Locate every parasitized RBC.
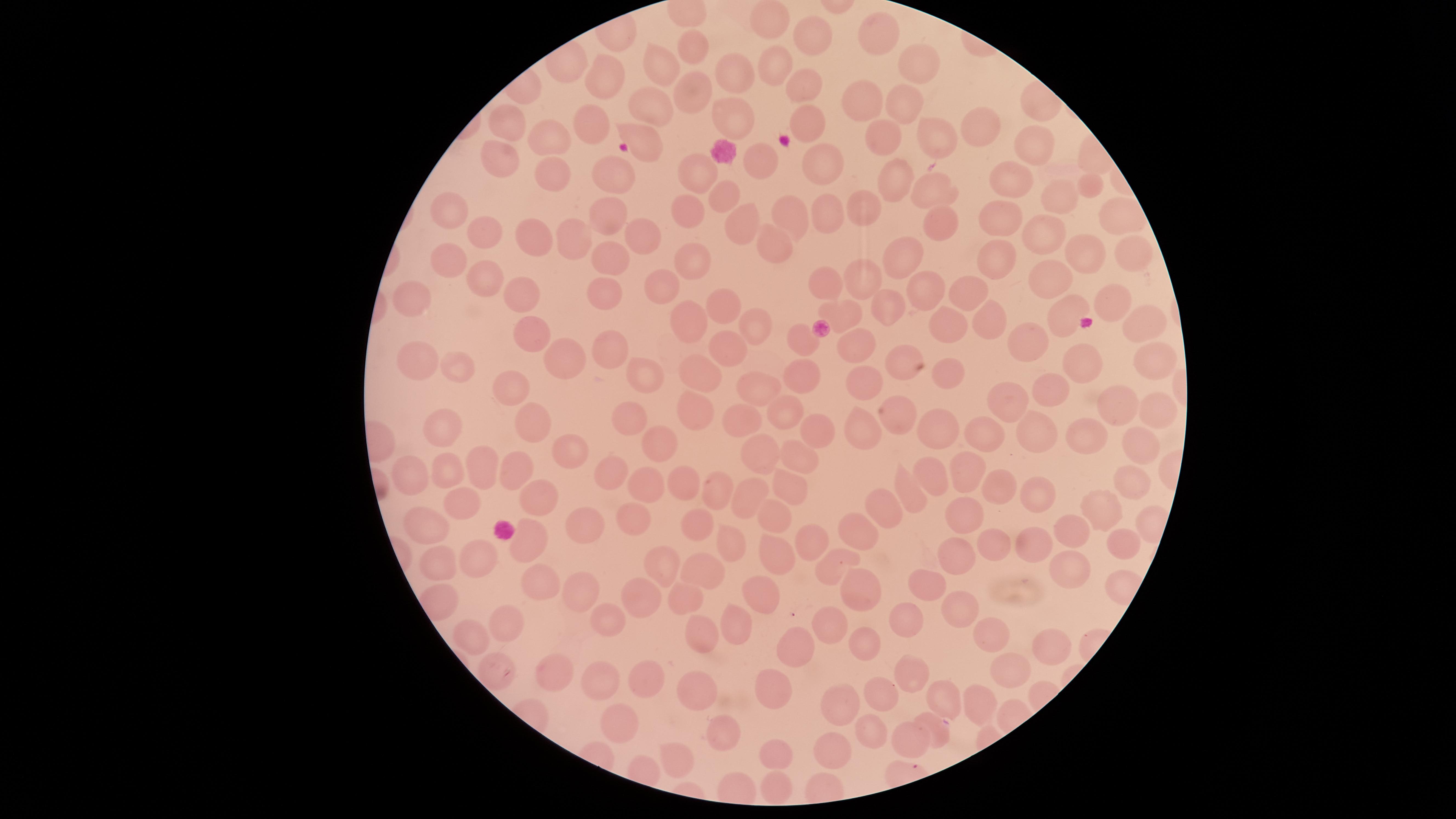

Approximate marker points as {x, y} in pixels.
Parasitized RBCs: {936, 729}.

Approximate marker points as {x, y} in pixels. Uninfected RBCs: {768, 20}, {882, 32}, {815, 36}, {690, 44}, {914, 61}, {657, 64}, {774, 67}, {724, 75}, {598, 79}, {804, 82}, {691, 91}, {865, 95}, {902, 99}, {646, 105}, {727, 119}, {513, 121}, {810, 122}, {592, 126}, {976, 126}, {885, 137}, {548, 139}, {1033, 139}, {940, 140}, {650, 141}, {499, 151}, {760, 158}, {823, 161}, {553, 171}, {700, 176}, {895, 176}, {619, 180}, {1016, 184}, {1087, 184}, {944, 188}, {726, 198}, {1062, 199}, {452, 205}, {868, 205}, {798, 207}, {690, 208}, {827, 208}, {1003, 211}, {599, 213}, {1120, 215}, {945, 219}, {745, 220}, {491, 230}, {1042, 233}, {640, 234}, {530, 235}, {780, 239}, {577, 242}, {1131, 242}, {452, 252}, {1079, 252}, {902, 253}, {613, 258}, {696, 263}, {1003, 264}, {481, 273}, {866, 273}, {1055, 278}, {828, 284}, {660, 286}, {924, 286}, {512, 290}, {975, 292}, {409, 295}, {601, 296}, {1116, 302}, {715, 306}, {885, 307}, {850, 308}, {1063, 309}, {992, 315}, {756, 318}, {1139, 319}, {691, 321}, {952, 321}, {531, 336}, {1037, 340}, {803, 341}, {729, 343}, {864, 344}, {614, 348}, {902, 358}, {1157, 358}, {568, 359}, {418, 362}, {459, 363}, {1090, 363}, {703, 369}, {952, 370}, {648, 372}, {807, 373}, {864, 380}, {511, 385}, {757, 385}, {1050, 388}, {1114, 404}, {1010, 407}, {697, 410}, {1157, 410}, {788, 413}, {900, 416}, {622, 419}, {439, 421}, {539, 421}, {742, 421}, {935, 428}, {860, 429}, {1088, 429}, {816, 434}, {1032, 434}, {986, 437}, {1132, 440}, {658, 442}, {566, 451}, {762, 453}, {799, 453}, {478, 463}, {964, 469}, {932, 470}, {614, 471}, {509, 473}, {1129, 473}, {443, 474}, {415, 475}, {679, 475}, {645, 481}, {996, 481}, {786, 484}, {712, 489}, {1038, 492}, {906, 493}, {746, 498}, {466, 505}, {538, 505}, {882, 507}, {1103, 508}, {966, 514}, {635, 517}, {780, 517}, {701, 525}, {428, 526}, {1081, 526}, {579, 527}, {858, 532}, {729, 537}, {812, 538}, {1120, 541}, {520, 542}, {994, 543}, {1038, 548}, {772, 557}, {475, 559}, {955, 559}, {664, 562}, {439, 565}, {826, 565}, {701, 569}, {1068, 569}, {536, 581}, {926, 583}, {853, 585}, {579, 587}, {647, 589}, {762, 590}, {680, 595}, {962, 603}, {612, 617}, {832, 623}, {904, 623}, {511, 625}, {734, 625}, {475, 634}, {995, 637}, {693, 638}, {1048, 640}, {864, 643}, {797, 649}, {498, 672}, {553, 673}, {1009, 674}, {595, 679}, {646, 679}, {909, 679}, {698, 687}, {773, 689}, {879, 696}, {943, 696}, {840, 701}, {984, 704}, {625, 715}, {869, 724}, {723, 731}, {910, 739}, {834, 748}, {678, 755}, {778, 755}, {779, 785}. Circular visible region. One field of view of the specimen. Giemsa stain. Image is 1456×819 pixels. Thin blood film. Photographed with a smartphone camera through the microscope eyepiece. Species: Plasmodium falciparum.